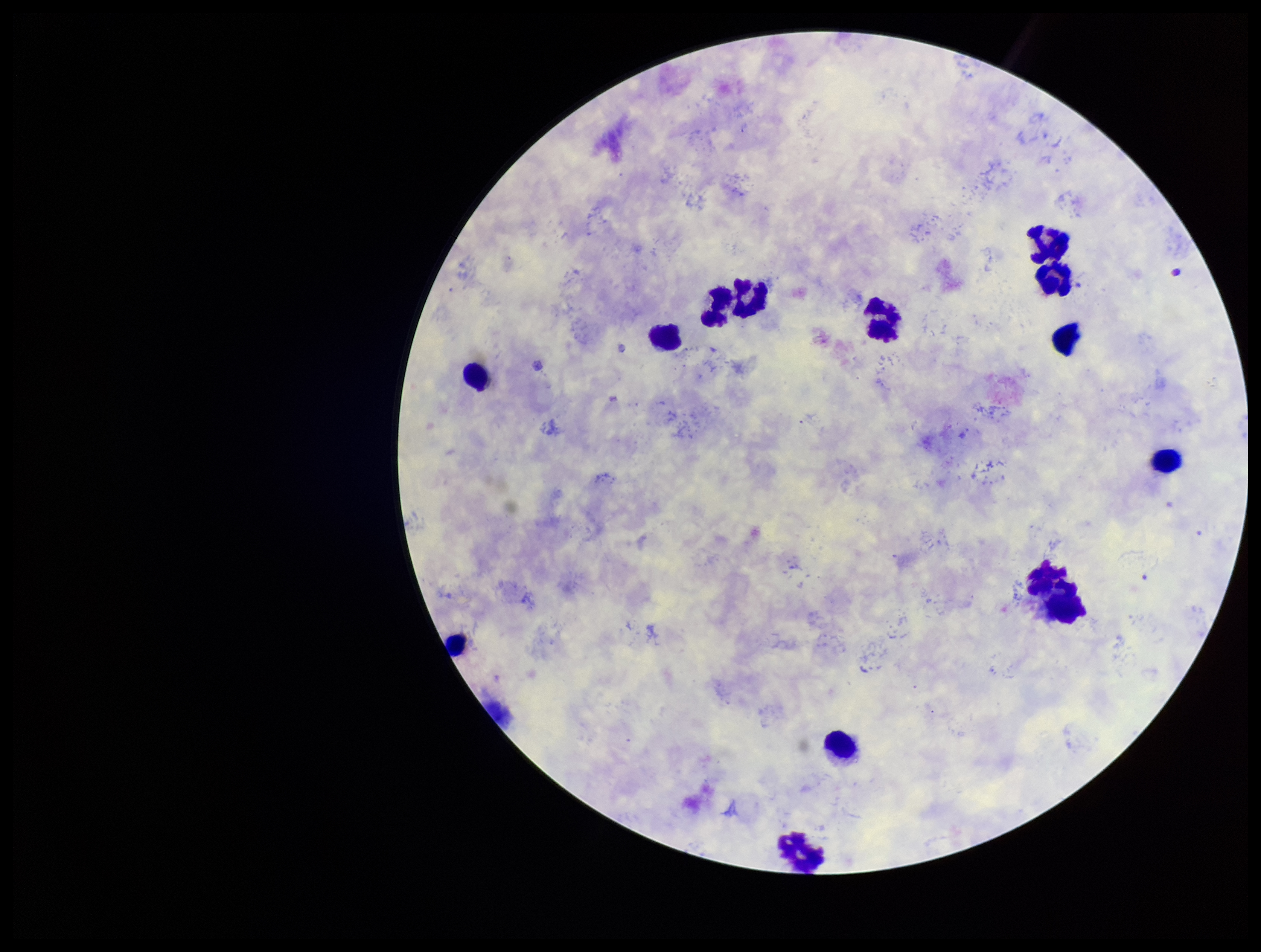

Plasmodium parasites = none detected
stain = Giemsa
preparation = thick smear
capture = smartphone photograph through the microscope eyepiece
image size = 1261×952 pixels
patient malaria status = infected
leukocyte count = 13
parasite count = 0
field of view = one from this slide
species reported for this patient = Plasmodium vivax